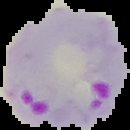
Summary:
  - Result: malaria parasites identified
  - Image size: 130×130 pixels
  - Preparation: thin blood smear
  - Image type: cell region segmented out of the field of view; surrounding area masked to black